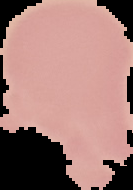
The area outside the segmented cell region is set to black. Image is 133×190 pixels. From a thin blood smear. Malaria status: uninfected.